Name the parasite shown.
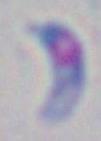

This is Toxoplasma gondii.

1000x magnification. Photomicrograph.